Outline each Plasmodium falciparum-infected red blood cell.
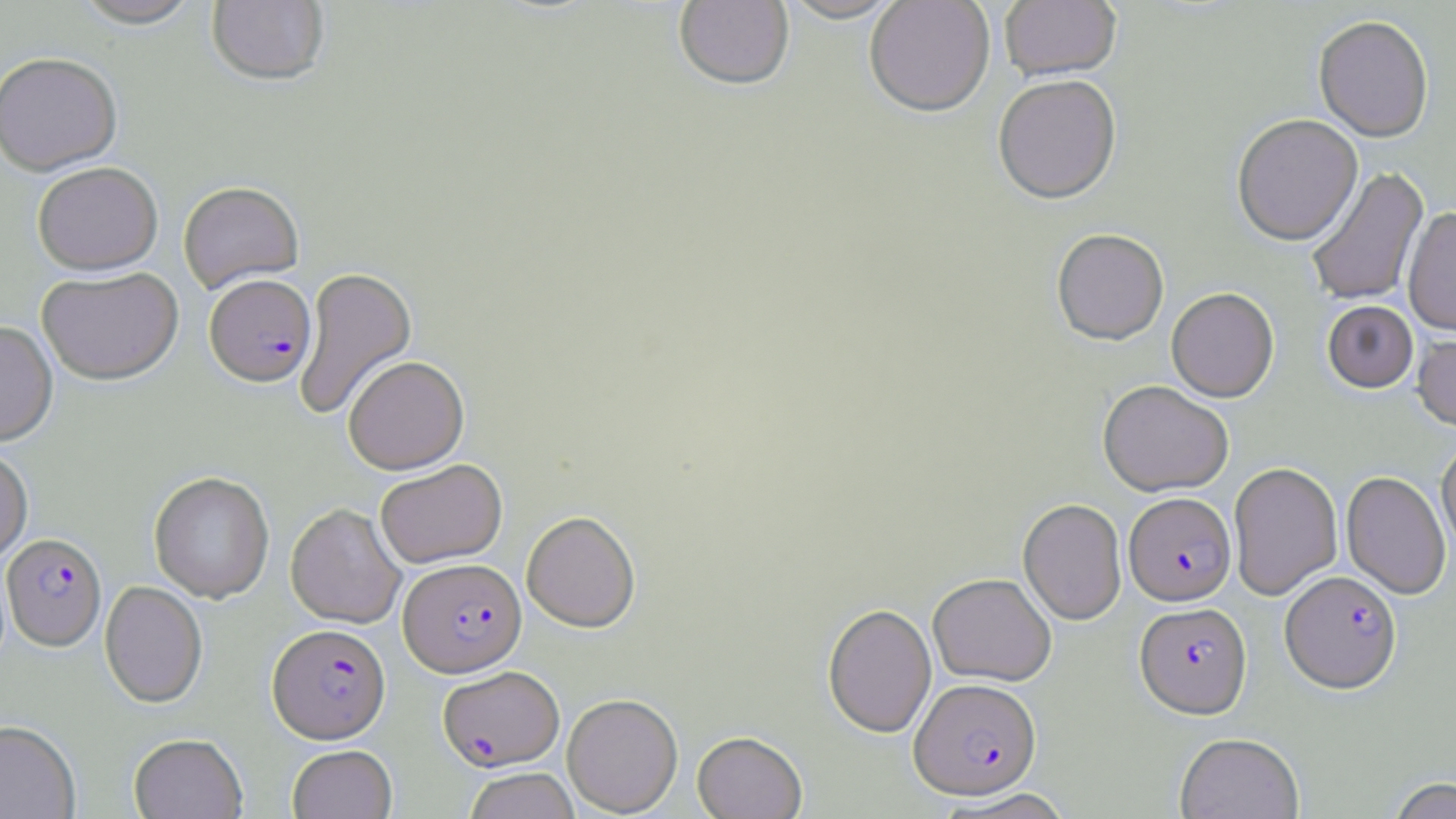
Approximate bounding boxes as named x1/y1/x2/y2 corners in pixels.
Plasmodium falciparum-infected red blood cells: (x1=204, y1=275, x2=316, y2=387), (x1=1123, y1=496, x2=1237, y2=609), (x1=2, y1=533, x2=106, y2=651), (x1=398, y1=558, x2=527, y2=677), (x1=1279, y1=573, x2=1403, y2=698), (x1=1134, y1=604, x2=1252, y2=722), (x1=267, y1=624, x2=391, y2=744), (x1=437, y1=666, x2=564, y2=772), (x1=909, y1=680, x2=1043, y2=802).

slide-level diagnosis = Plasmodium falciparum
preparation = thin blood smear
uninfected red blood cell locations = approximate bounding boxes as named x1/y1/x2/y2 corners in pixels: (x1=71, y1=0, x2=203, y2=31), (x1=207, y1=0, x2=330, y2=88), (x1=673, y1=0, x2=794, y2=93), (x1=778, y1=0, x2=907, y2=26), (x1=865, y1=0, x2=995, y2=120), (x1=999, y1=0, x2=1121, y2=84), (x1=1313, y1=18, x2=1433, y2=146), (x1=0, y1=53, x2=123, y2=177), (x1=994, y1=78, x2=1121, y2=208), (x1=1232, y1=116, x2=1363, y2=249), (x1=32, y1=162, x2=163, y2=275), (x1=1307, y1=167, x2=1430, y2=307), (x1=178, y1=180, x2=304, y2=293), (x1=1402, y1=210, x2=1456, y2=338), (x1=1051, y1=231, x2=1169, y2=348), (x1=294, y1=266, x2=417, y2=422), (x1=37, y1=267, x2=184, y2=386), (x1=1167, y1=290, x2=1279, y2=405), (x1=1322, y1=302, x2=1418, y2=396), (x1=0, y1=321, x2=58, y2=448), (x1=1412, y1=332, x2=1456, y2=434), (x1=343, y1=355, x2=470, y2=474), (x1=1097, y1=383, x2=1233, y2=500), (x1=1436, y1=443, x2=1456, y2=558), (x1=0, y1=445, x2=33, y2=566), (x1=375, y1=459, x2=507, y2=568), (x1=1228, y1=464, x2=1343, y2=602), (x1=149, y1=472, x2=275, y2=604), (x1=1340, y1=473, x2=1451, y2=600), (x1=1017, y1=500, x2=1127, y2=627), (x1=285, y1=503, x2=406, y2=629), (x1=522, y1=511, x2=640, y2=633), (x1=927, y1=575, x2=1057, y2=687), (x1=100, y1=581, x2=208, y2=708), (x1=822, y1=604, x2=937, y2=739), (x1=562, y1=693, x2=683, y2=816), (x1=0, y1=720, x2=81, y2=818), (x1=692, y1=732, x2=807, y2=819), (x1=129, y1=733, x2=247, y2=819), (x1=1174, y1=735, x2=1304, y2=819), (x1=287, y1=745, x2=398, y2=819), (x1=463, y1=768, x2=581, y2=819), (x1=1386, y1=778, x2=1456, y2=819), (x1=938, y1=789, x2=1077, y2=819)
field of view = single
image size = 1456×819 pixels
magnification = 1000x
stain = May-Grünwald-Giemsa
modality = optical microscopy